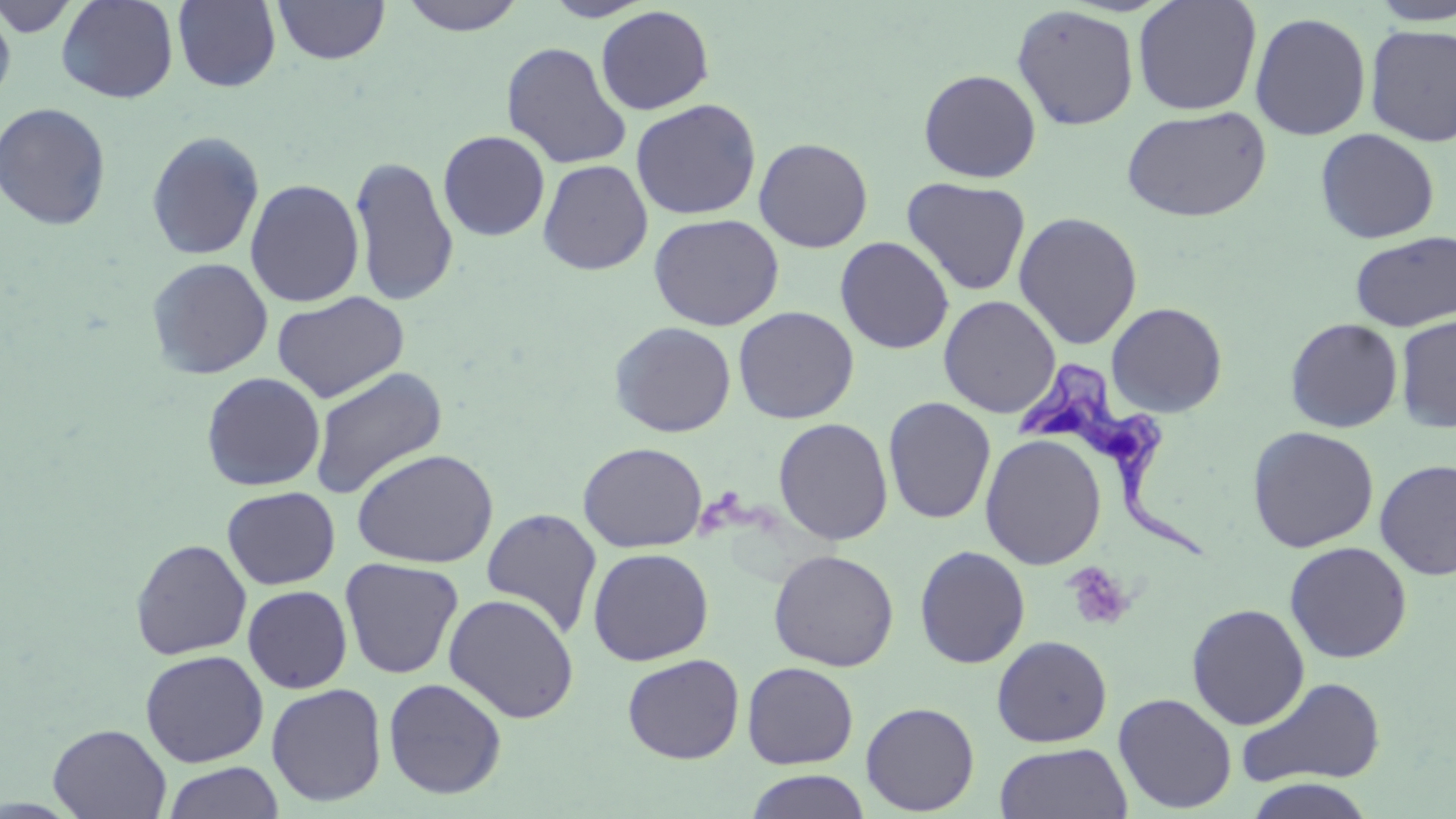

{
  "slide_level_diagnosis": "Trypanosoma brucei",
  "platelet_locations": "approximate bounding boxes as [x1, y1, x2, y2] in pixels: [1063, 562, 1135, 632]",
  "trypanosoma_brucei_locations": "approximate bounding boxes as [x1, y1, x2, y2] in pixels: [1016, 361, 1204, 561]",
  "field_of_view": "one of a larger specimen",
  "preparation": "thin blood smear",
  "modality": "light microscopy",
  "image_size": "1456×819 pixels",
  "uninfected_red_blood_cell_locations": "approximate bounding boxes as [x1, y1, x2, y2] in pixels: [1, 0, 83, 38], [56, 0, 179, 104], [273, 0, 390, 65], [397, 0, 529, 35], [542, 0, 655, 21], [172, 1, 281, 91], [1132, 1, 1263, 116], [1369, 1, 1456, 26], [0, 3, 17, 111], [595, 5, 715, 115], [1011, 5, 1140, 131], [1249, 12, 1371, 141], [1364, 25, 1456, 146], [500, 41, 632, 169], [918, 69, 1041, 182], [630, 98, 761, 219], [0, 102, 112, 230], [1120, 105, 1272, 223], [1315, 128, 1440, 244], [437, 130, 551, 242], [145, 131, 265, 261], [753, 137, 874, 253], [349, 156, 459, 307], [538, 159, 653, 275], [901, 177, 1031, 297], [245, 179, 364, 307], [1013, 211, 1143, 350], [648, 213, 784, 331], [1350, 231, 1456, 331], [834, 236, 955, 355], [146, 257, 273, 379], [272, 291, 410, 404], [938, 295, 1061, 418], [1106, 302, 1228, 417], [733, 306, 859, 424], [1274, 315, 1393, 550], [1395, 315, 1456, 434], [1285, 317, 1403, 432], [609, 321, 736, 437], [308, 366, 448, 500], [201, 372, 326, 492], [883, 397, 996, 524], [773, 417, 893, 545], [1247, 425, 1379, 552], [980, 433, 1107, 570], [578, 442, 707, 552], [351, 448, 498, 569], [1375, 459, 1456, 580], [222, 486, 340, 590], [481, 508, 602, 640], [130, 539, 252, 660], [1284, 541, 1412, 663], [914, 545, 1031, 668], [587, 547, 714, 666], [768, 549, 899, 671], [339, 557, 464, 680], [242, 585, 352, 693], [443, 593, 580, 723], [1186, 603, 1310, 730], [992, 635, 1112, 747], [140, 650, 268, 767], [622, 653, 745, 764], [742, 661, 859, 769], [1235, 676, 1387, 788], [383, 677, 507, 799], [266, 682, 387, 807], [1113, 692, 1237, 814], [861, 701, 980, 815], [47, 724, 171, 818], [993, 742, 1132, 819], [162, 762, 285, 819], [744, 769, 872, 819], [1243, 778, 1377, 819]",
  "stain": "May-Grünwald-Giemsa",
  "magnification": "1000x"
}